Report the malaria status of this cell.
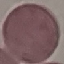

It is uninfected.

Photographed with a smartphone camera at the microscope eyepiece. Automatically extracted cell patch, resized to 64 × 64 pixels. Giemsa stain. Thin blood smear.